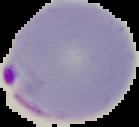

preparation = thin blood film
malaria status = parasitized
image size = 139×127 pixels
image type = cell region segmented out of the field of view; surrounding area masked to black